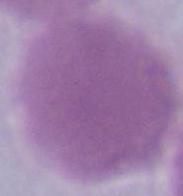
{
  "magnification": "1000x",
  "modality": "micrograph",
  "identification": "erythrocyte"
}